Classify this cell by malaria status.
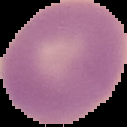

It is uninfected.

image_size: 127×127 pixels
preparation: thin blood film
image_type: segmented cell region on a black background